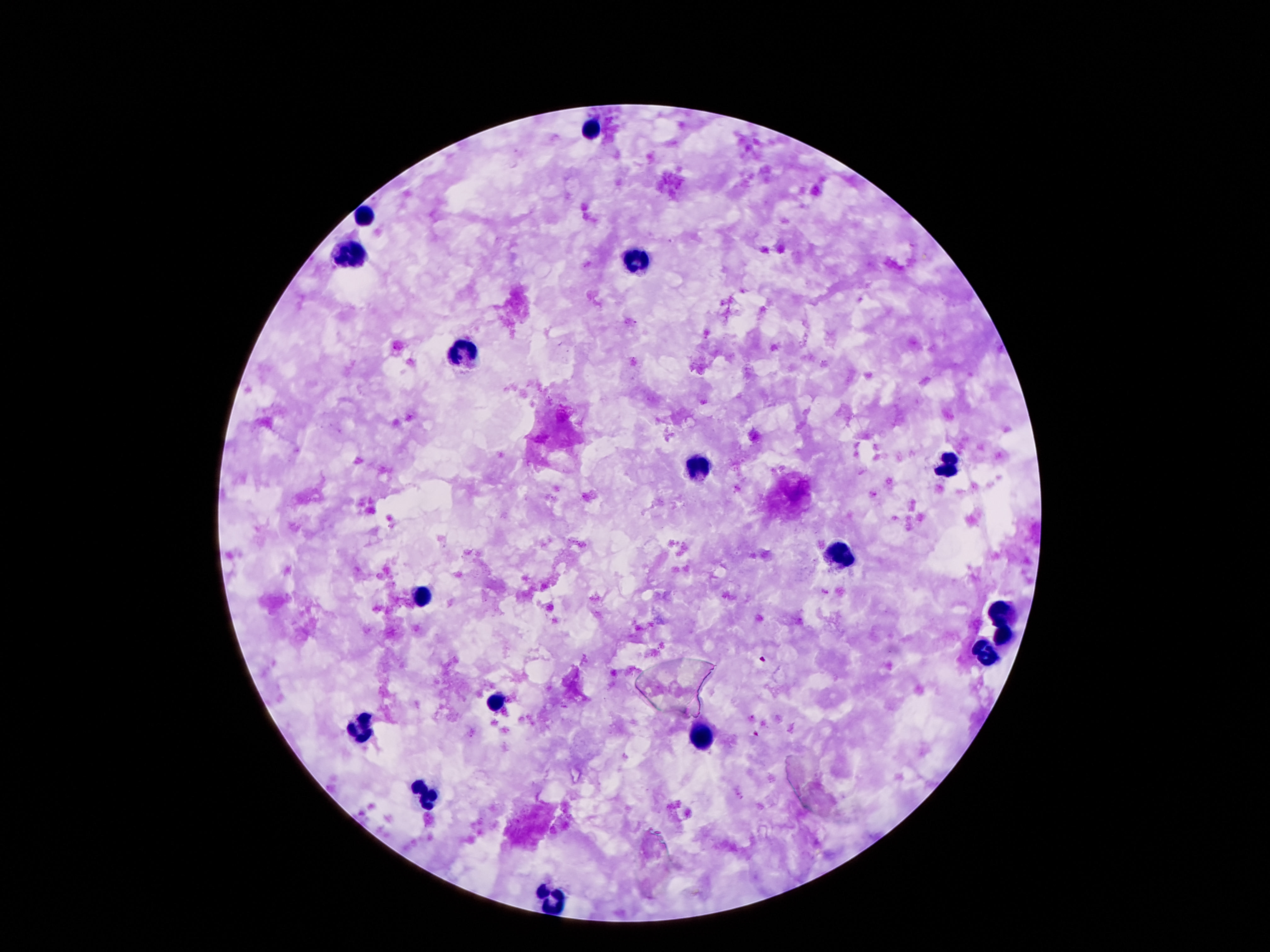

Approximate centers as (x, y) in pixels. Leukocyte locations: (591, 128), (365, 212), (353, 253), (632, 261), (468, 356), (947, 468), (697, 470), (837, 556), (419, 597), (1005, 610), (1003, 634), (984, 655), (497, 704), (361, 730), (699, 737), (427, 795), (550, 900). Smartphone photograph taken through the microscope eyepiece. Patient malaria status: uninfected. Giemsa-stained preparation. Thick peripheral-blood smear. Single field of view. Image is 1270×952 pixels. 100x magnification.